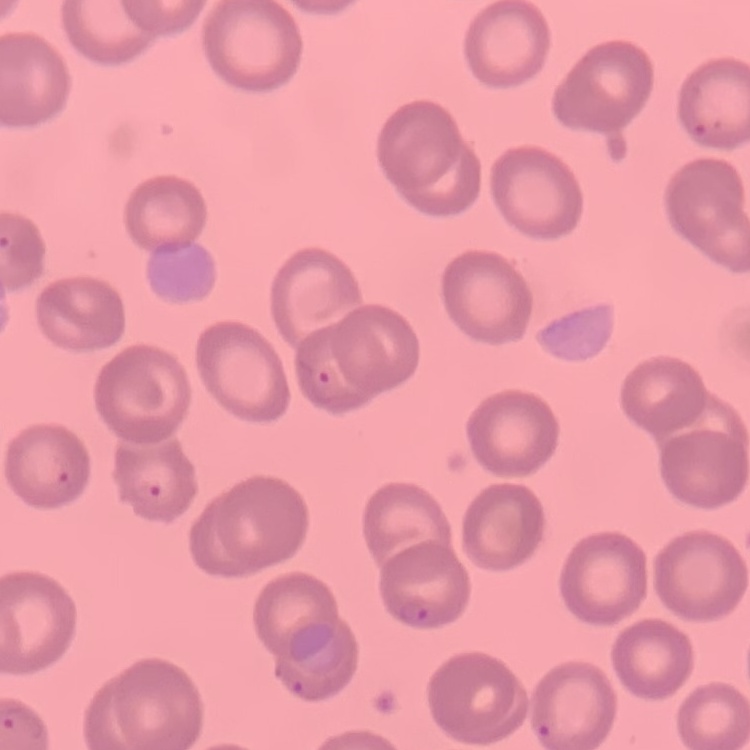

Summary:
  - Erythrocyte morphology: no rouleaux formation
  - Stain: Field's or Giemsa
  - Image type: one tile cut from a larger photomicrograph
  - Preparation: thin blood film